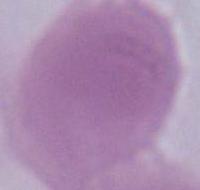

identification: erythrocyte
modality: photomicrograph
magnification: 1000x